Name the cell type shown.
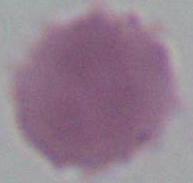
This is an erythrocyte.

Summary:
  - Modality: photomicrograph
  - Magnification: 1000x